Name the parasite shown.
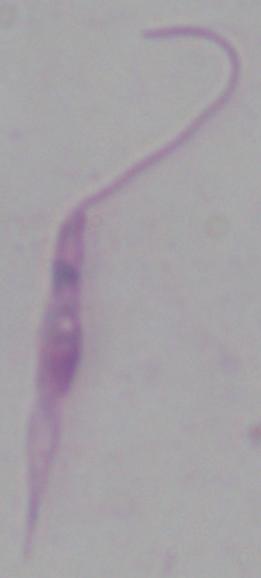
Leishmania.

Summary:
  - Magnification: 1000x
  - Modality: photomicrograph